Comment on the morphology of the erythrocytes.
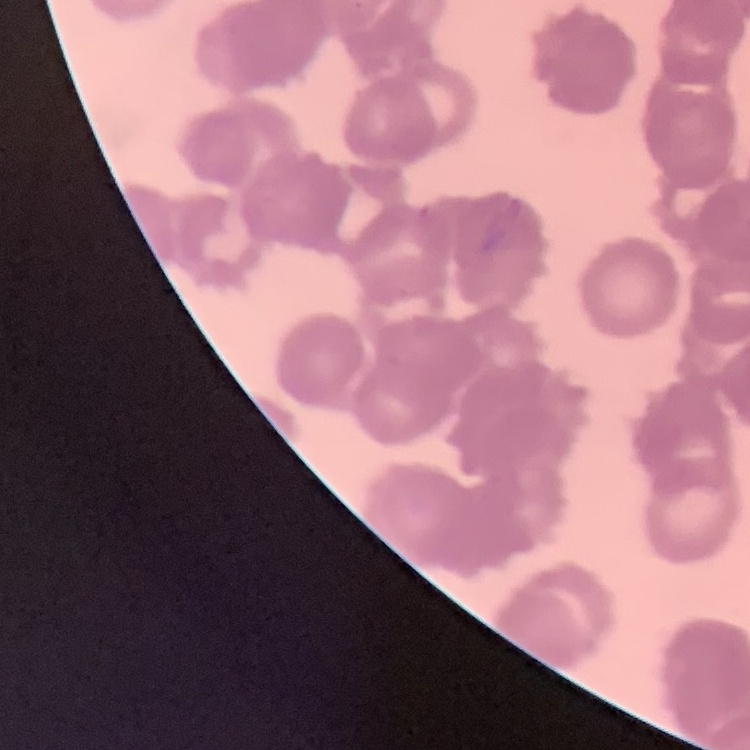
They show rouleaux formation.

stain: Field's or Giemsa
image_type: one tile cut from a larger photomicrograph
preparation: thin blood film